Locate every blood parasite and identify its species.
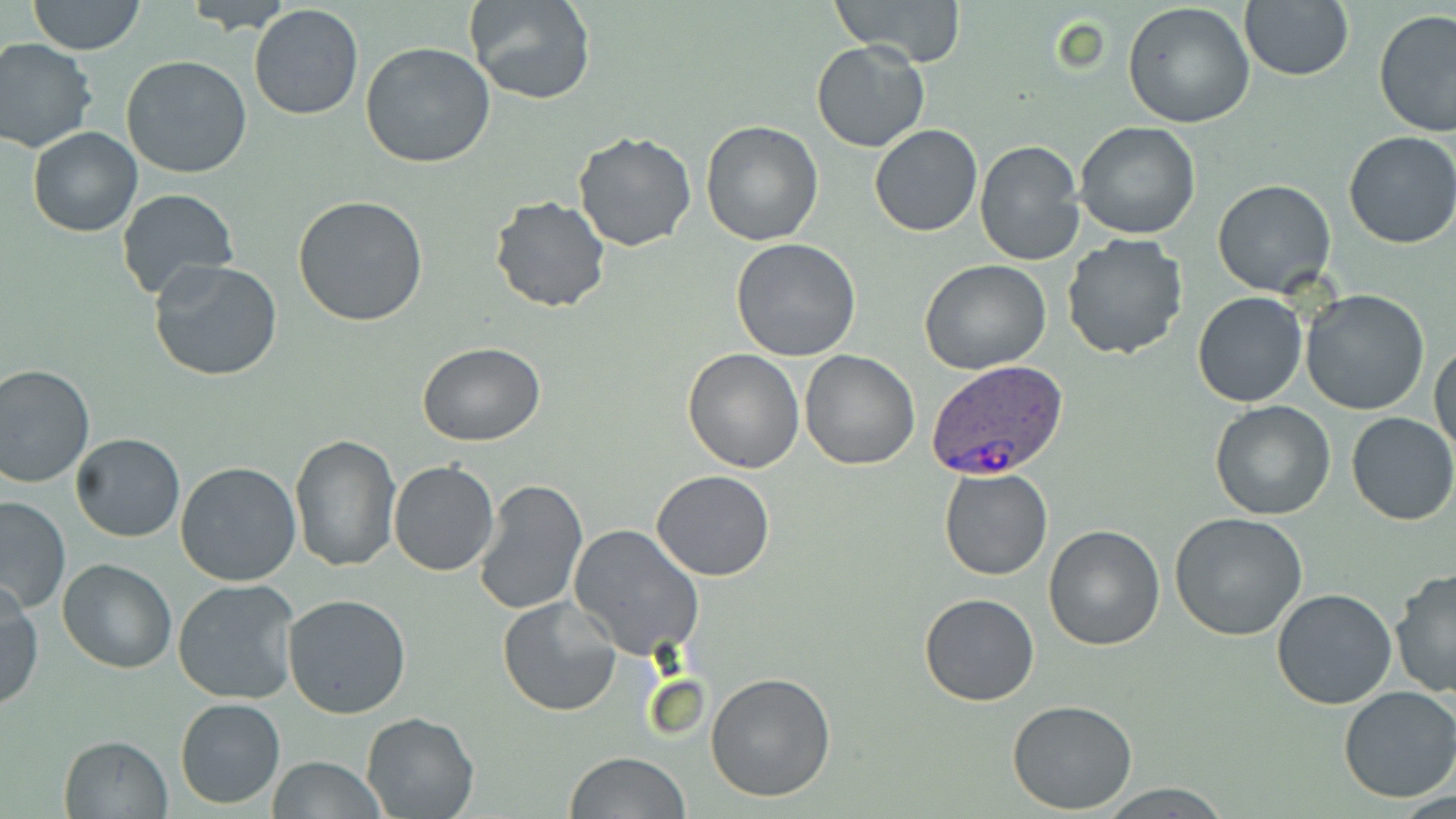

Approximate bounding boxes as (x1,y1)-(x2,y2) corner pairs in pixels.
Plasmodium ovale-infected red blood cells: (927,359)-(1070,481).
No Plasmodium falciparum, Plasmodium malariae, Plasmodium vivax, Babesia divergens, or Trypanosoma brucei observed.

Summary:
  - Uninfected red blood cell locations: (27,0)-(145,55), (181,0)-(295,34), (465,0)-(596,105), (838,0)-(965,66), (1239,2)-(1355,82), (1121,3)-(1256,130), (247,4)-(364,121), (1372,10)-(1456,140), (0,37)-(98,153), (810,41)-(929,153), (359,43)-(497,169), (121,54)-(253,179), (699,120)-(824,247), (1074,122)-(1200,239), (869,124)-(982,237), (28,127)-(141,237), (574,131)-(696,251), (1342,132)-(1456,249), (974,139)-(1084,267), (1212,179)-(1337,297), (116,188)-(239,300), (292,195)-(428,327), (489,195)-(612,313), (1060,233)-(1187,360), (729,238)-(861,360), (148,259)-(283,382), (918,259)-(1052,373), (1300,288)-(1432,415), (1191,292)-(1307,408), (1431,338)-(1456,457), (417,343)-(547,447), (682,348)-(805,474), (799,349)-(920,470), (0,361)-(96,488), (1208,401)-(1336,521), (1347,411)-(1456,526), (71,433)-(185,542), (289,433)-(401,572), (175,460)-(304,587), (388,461)-(500,577), (939,468)-(1053,581), (651,470)-(777,580), (473,480)-(588,616), (0,496)-(70,617), (1169,513)-(1310,642), (1042,523)-(1166,650), (567,524)-(704,660), (58,559)-(177,673), (1389,567)-(1456,701), (173,578)-(304,706), (0,582)-(42,712), (1271,589)-(1397,710), (282,592)-(413,719), (917,593)-(1041,707), (497,596)-(621,717), (705,672)-(837,802), (1337,685)-(1456,803), (174,697)-(285,808), (1007,699)-(1138,815), (361,712)-(481,819), (58,734)-(174,819), (565,751)-(692,819), (268,756)-(385,819)
  - Slide-level diagnosis: Plasmodium ovale
  - Image size: 1456×819 pixels
  - Field of view: one of a larger specimen
  - Modality: light microscopy
  - Preparation: thin blood smear
  - Stain: May-Grünwald-Giemsa
  - Magnification: 1000x